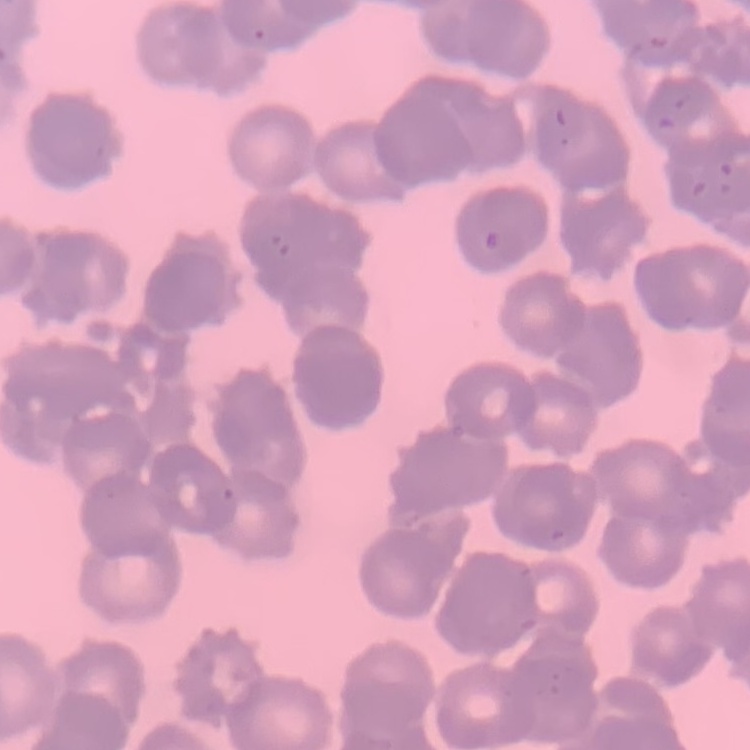 The red blood cells exhibit rouleaux formation. Stained with either Field's or Giemsa. Square crop of a larger photomicrograph. Thin blood smear.